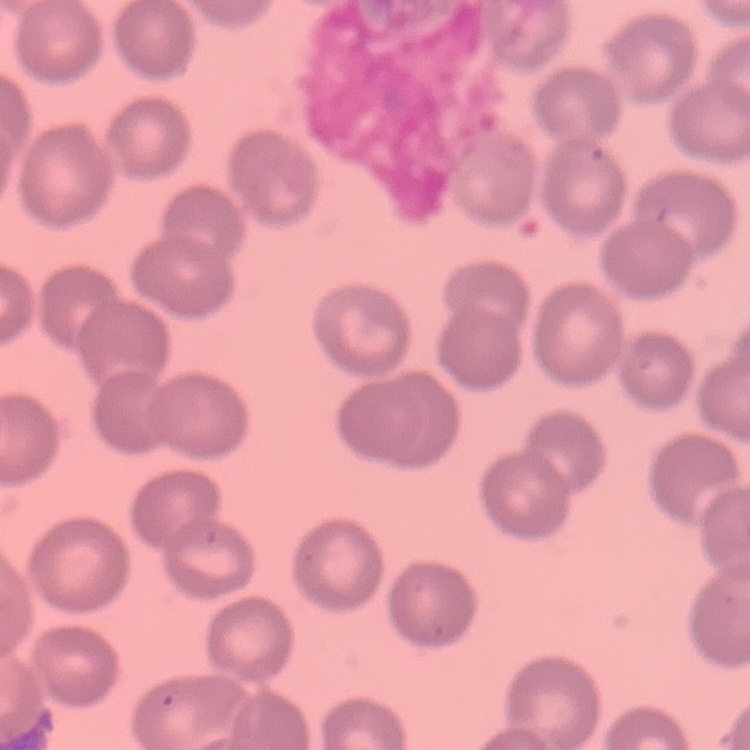
The red blood cells show no rouleaux formation. Field's or Giemsa stain. Square crop of a larger photomicrograph. Thin blood smear.